Describe the morphology of the red blood cells.
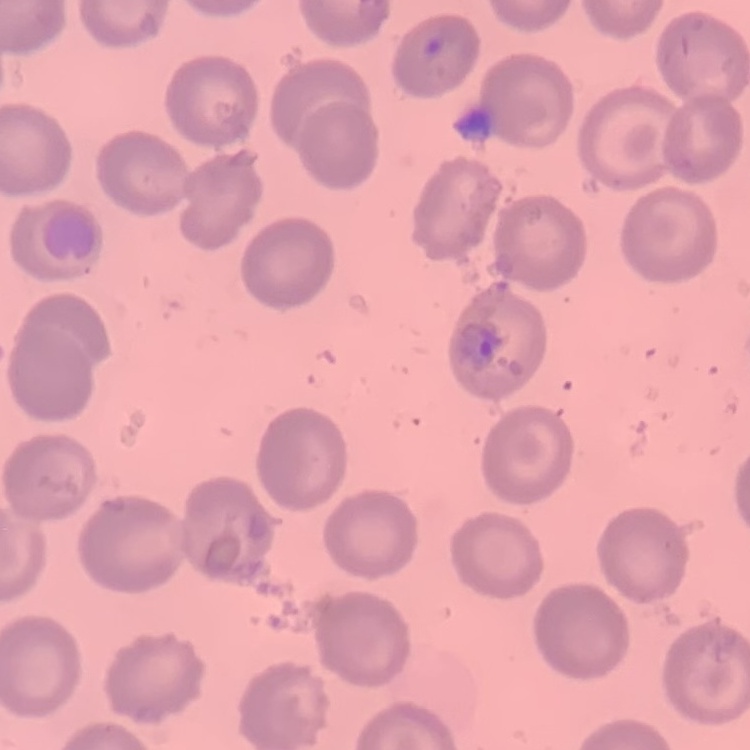

They show no rouleaux formation.

Summary:
  - Stain: Field's or Giemsa
  - Preparation: thin blood film
  - Image type: square crop of a larger photomicrograph